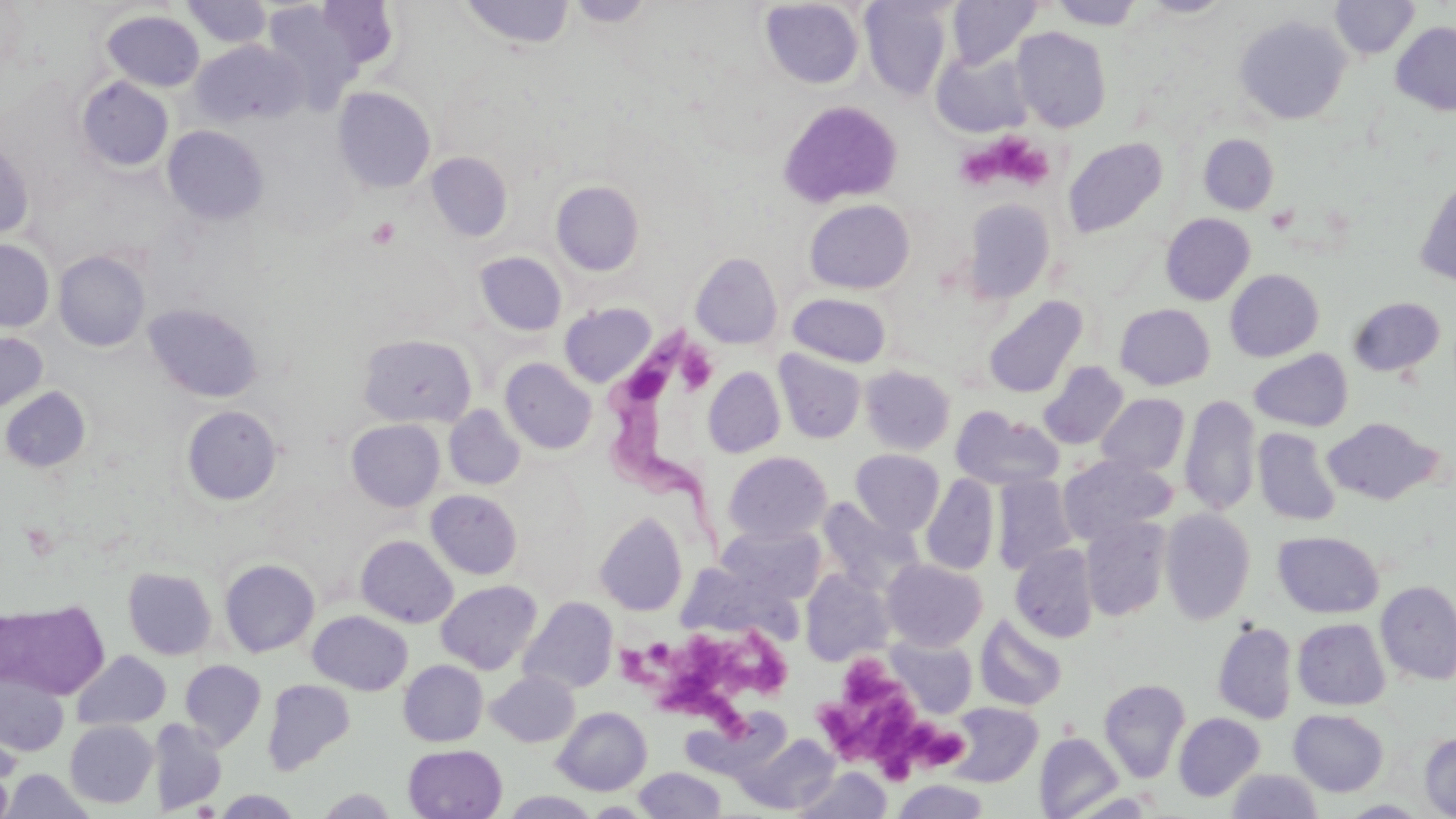
Approximate bounding boxes as [x1, y1, x2, y2] in pixels. Platelet locations: [993, 136, 1054, 188], [959, 143, 1004, 192], [366, 217, 402, 249], [677, 348, 716, 394], [713, 627, 795, 708], [657, 631, 729, 721], [622, 637, 676, 683], [842, 656, 905, 711], [704, 692, 748, 735], [814, 694, 917, 766], [902, 723, 945, 761], [929, 734, 963, 769], [879, 747, 917, 788]. Trypanosoma brucei locations: [605, 320, 716, 560]. Uninfected red blood cell locations: [260, 0, 392, 108], [458, 0, 574, 50], [566, 0, 657, 28], [946, 0, 1042, 69], [1139, 0, 1234, 18], [1330, 0, 1419, 59], [181, 1, 272, 49], [760, 1, 864, 89], [859, 1, 954, 100], [1050, 1, 1144, 30], [102, 10, 205, 92], [1234, 14, 1352, 125], [1391, 21, 1456, 116], [1012, 26, 1112, 132], [192, 39, 305, 127], [932, 47, 1034, 137], [76, 76, 174, 173], [333, 86, 436, 194], [779, 100, 902, 208], [162, 125, 268, 226], [1199, 134, 1278, 214], [0, 136, 34, 241], [1063, 138, 1168, 237], [426, 151, 512, 243], [1414, 179, 1456, 287], [550, 180, 644, 276], [961, 198, 1056, 303], [804, 199, 915, 294], [1161, 213, 1255, 305], [0, 239, 54, 333], [54, 250, 151, 352], [474, 251, 567, 337], [690, 252, 783, 349], [1225, 269, 1323, 362], [788, 293, 892, 367], [982, 295, 1088, 398], [1347, 296, 1446, 377], [560, 302, 657, 387], [144, 303, 263, 403], [1114, 303, 1215, 390], [0, 332, 47, 414], [357, 333, 477, 428], [1250, 349, 1352, 431], [774, 350, 866, 444], [500, 358, 597, 454], [1039, 361, 1129, 450], [859, 365, 956, 455], [703, 366, 786, 458], [1, 386, 91, 473], [1097, 393, 1189, 477], [1179, 395, 1260, 516], [181, 405, 282, 505], [444, 405, 525, 490], [950, 406, 1063, 491], [1322, 417, 1441, 505], [346, 419, 445, 512], [1253, 428, 1342, 526], [850, 449, 945, 535], [723, 451, 832, 544], [1058, 455, 1175, 544], [921, 474, 999, 576], [992, 474, 1077, 575], [427, 490, 523, 579], [816, 498, 923, 594], [1160, 508, 1256, 625], [595, 511, 688, 616], [1080, 517, 1171, 621], [717, 524, 825, 603], [1273, 530, 1384, 618], [356, 535, 458, 628], [1010, 544, 1099, 642], [219, 558, 320, 657], [883, 559, 987, 650], [675, 561, 803, 643], [123, 567, 217, 661], [800, 569, 894, 666], [436, 579, 542, 674], [1375, 579, 1456, 685], [519, 597, 617, 695], [0, 598, 109, 698], [307, 610, 413, 695], [975, 614, 1067, 711], [1293, 618, 1390, 710], [1212, 620, 1298, 724], [885, 635, 979, 718], [72, 650, 171, 730], [179, 659, 267, 750], [399, 660, 488, 747], [0, 670, 69, 755], [487, 670, 579, 747], [1099, 678, 1190, 782], [262, 679, 355, 774], [945, 702, 1042, 787], [553, 707, 652, 795], [688, 708, 790, 781], [1289, 710, 1388, 796], [1174, 712, 1265, 802], [151, 718, 227, 814], [65, 720, 158, 808], [1419, 731, 1456, 819], [1035, 732, 1124, 818], [736, 733, 841, 814], [403, 744, 507, 819], [0, 757, 15, 819], [794, 766, 892, 819], [633, 767, 727, 818], [2, 769, 95, 818], [1226, 769, 1323, 818], [891, 778, 990, 819], [315, 788, 399, 817], [214, 790, 303, 818], [501, 791, 601, 818], [1341, 799, 1430, 818]. Slide-level diagnosis: Trypanosoma brucei. One field of a larger specimen. Thin blood film. 1000x magnification. Light microscopy. May-Grünwald-Giemsa-stained preparation. Image is 1456×819 pixels.